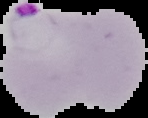
image type = segmented cell region with the area outside set to black
preparation = thin blood film
malaria status = parasitized
image size = 148×118 pixels